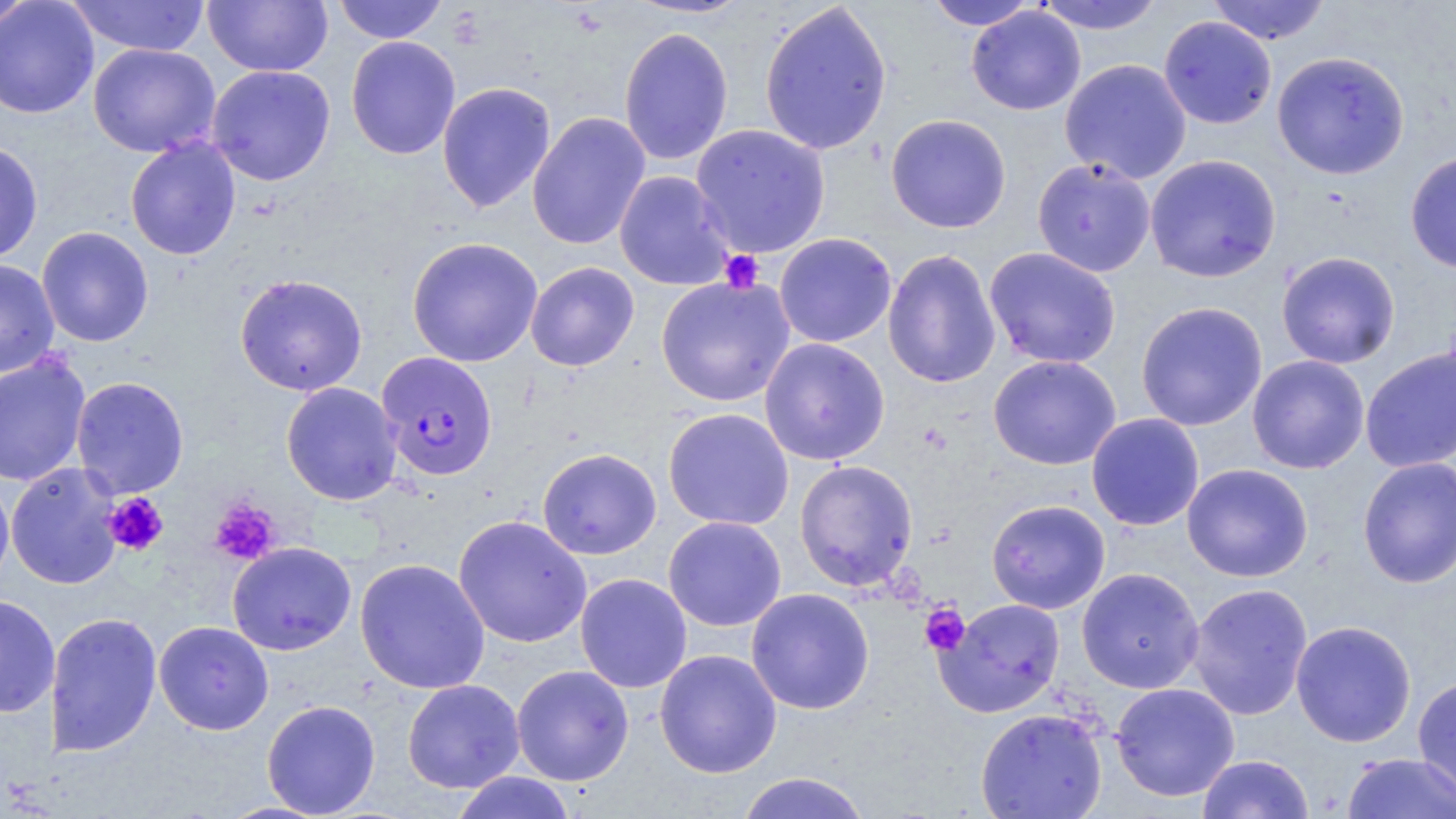
Summary:
  - Coordinate format: approximate bounding boxes as (x1, y1, x2, y2) in pixels
  - Platelet locations: (720, 250, 764, 293), (102, 492, 169, 556), (210, 498, 281, 565), (920, 604, 970, 655)
  - Uninfected red blood cell locations: (66, 0, 212, 57), (203, 0, 333, 77), (332, 0, 449, 43), (627, 0, 752, 19), (1034, 0, 1164, 35), (1207, 0, 1331, 45), (0, 1, 99, 119), (1, 1, 36, 31), (758, 1, 893, 156), (924, 1, 1042, 30), (966, 6, 1086, 115), (1158, 16, 1277, 129), (618, 26, 734, 166), (346, 35, 461, 160), (88, 43, 221, 157), (1272, 51, 1410, 179), (1060, 58, 1192, 184), (206, 65, 336, 186), (436, 81, 557, 213), (526, 111, 651, 250), (885, 113, 1011, 233), (690, 124, 830, 258), (124, 136, 242, 261), (0, 140, 43, 263), (1405, 151, 1456, 274), (1144, 154, 1282, 282), (1031, 158, 1156, 277), (614, 170, 736, 291), (36, 226, 154, 347), (774, 232, 897, 348), (406, 236, 543, 367), (984, 247, 1122, 369), (883, 249, 1001, 388), (1276, 251, 1401, 369), (0, 259, 59, 378), (525, 261, 640, 371), (234, 273, 368, 396), (656, 276, 795, 406), (1136, 301, 1267, 431), (759, 337, 890, 466), (1360, 346, 1456, 472), (0, 352, 91, 487), (988, 354, 1122, 470), (1247, 355, 1369, 473), (71, 376, 189, 498), (280, 382, 403, 505), (663, 408, 794, 531), (1085, 413, 1204, 531), (537, 448, 661, 559), (1357, 456, 1456, 588), (794, 460, 918, 591), (5, 462, 124, 590), (1182, 463, 1313, 582), (0, 474, 14, 596), (986, 499, 1110, 614), (453, 515, 592, 648), (663, 516, 786, 632), (227, 541, 356, 655), (354, 557, 490, 694), (1077, 567, 1204, 693), (575, 573, 692, 693), (1187, 582, 1313, 720), (746, 588, 875, 714), (0, 595, 60, 718), (936, 598, 1066, 718), (45, 611, 162, 757), (1290, 620, 1416, 747), (154, 621, 274, 735), (654, 649, 782, 778), (511, 664, 634, 786), (1412, 675, 1456, 805), (402, 679, 525, 793), (1110, 682, 1240, 801), (261, 700, 381, 817), (975, 708, 1107, 819), (1341, 752, 1456, 819), (1197, 753, 1314, 818), (450, 771, 578, 819), (735, 771, 873, 819)
  - Plasmodium falciparum-infected red blood cell locations: (376, 351, 499, 481)
  - Slide-level diagnosis: Plasmodium falciparum
  - Field of view: single
  - Preparation: thin blood smear
  - Image size: 1456×819 pixels
  - Magnification: 1000x
  - Stain: May-Grünwald-Giemsa
  - Modality: optical microscopy